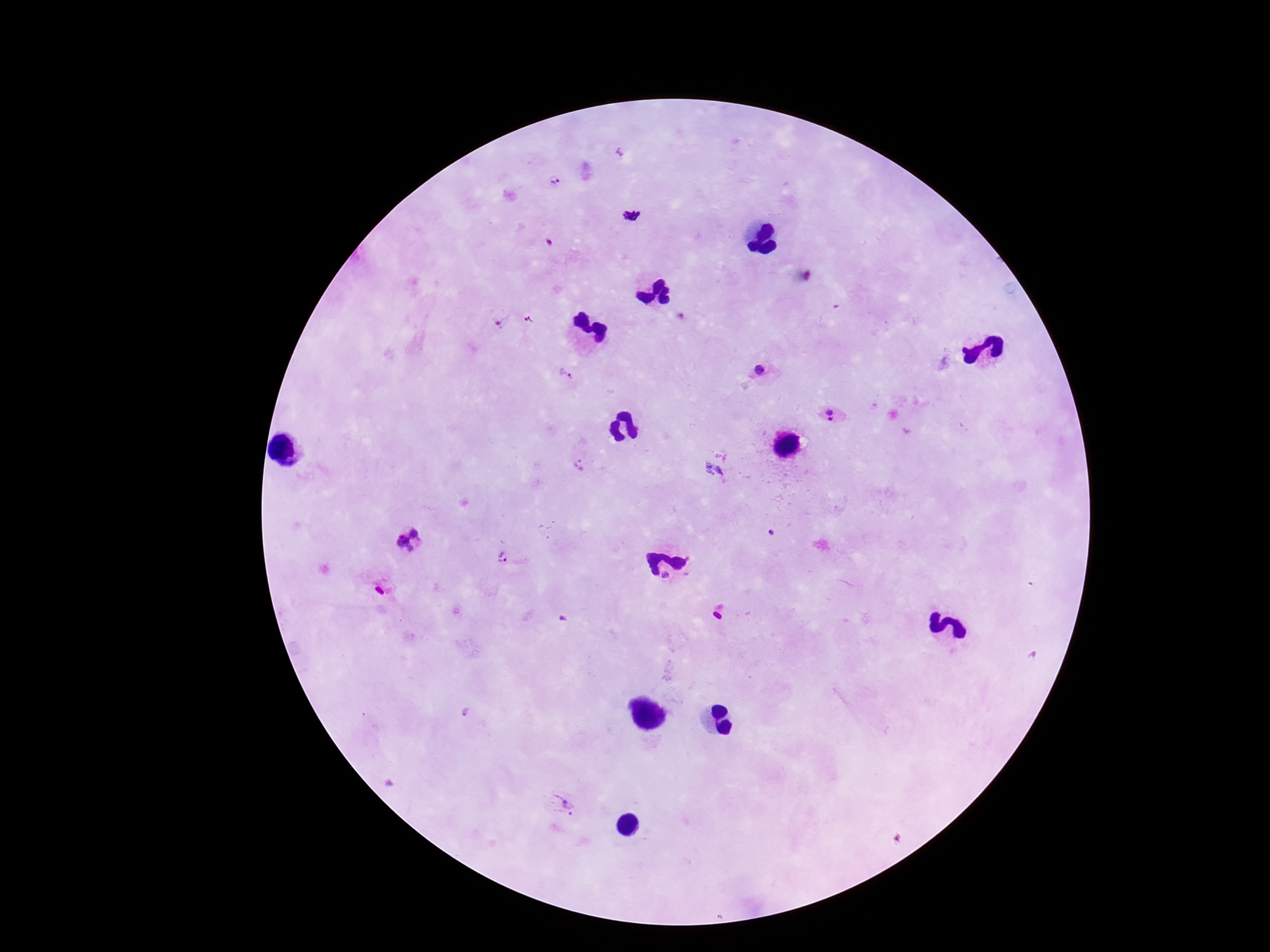 Approximate centers as [x, y] in pixels. Plasmodium parasite locations: [619, 152], [555, 181], [632, 217], [531, 318], [757, 372], [564, 374], [827, 416], [580, 465], [408, 540], [505, 559], [567, 803]. Single field of view. Giemsa-stained preparation. Image is 1270×952 pixels. Smartphone photograph taken through the microscope eyepiece. 100x magnification. Patient malaria status: infected. Thick peripheral-blood smear.